Describe the morphology of the erythrocytes.
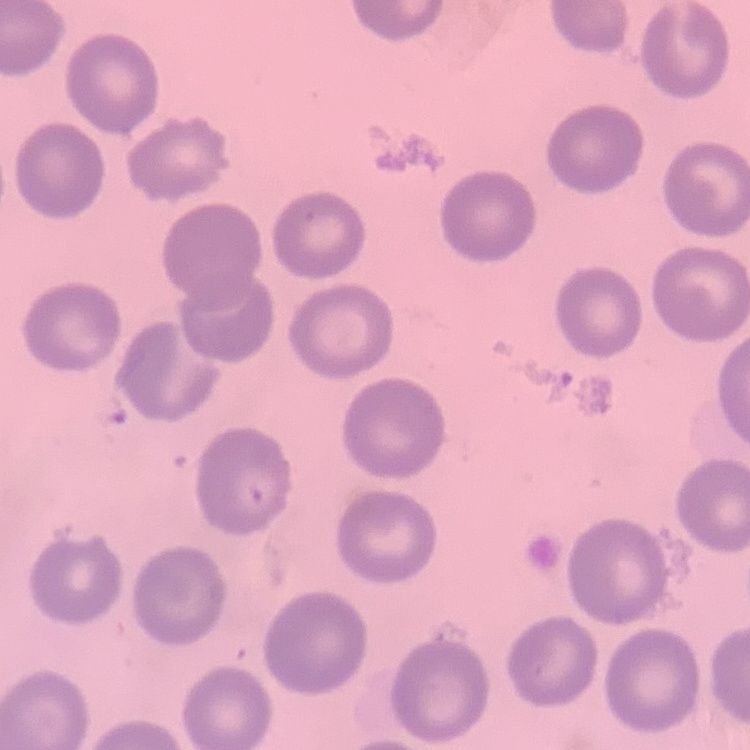

No rouleaux formation.

Summary:
  - Preparation: thin blood film
  - Stain: Field's or Giemsa
  - Image type: square crop of a larger photomicrograph